Report the malaria status of this cell.
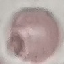

Uninfected.

Giemsa stain. Photographed with a smartphone camera at the microscope eyepiece. Automatically extracted cell patch, resized to 64 × 64 pixels. Thin blood film.